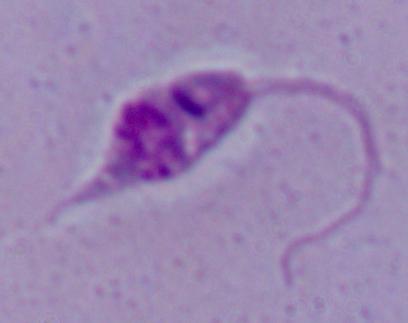
Summary:
  - Magnification: 1000x
  - Identification: Leishmania
  - Modality: micrograph